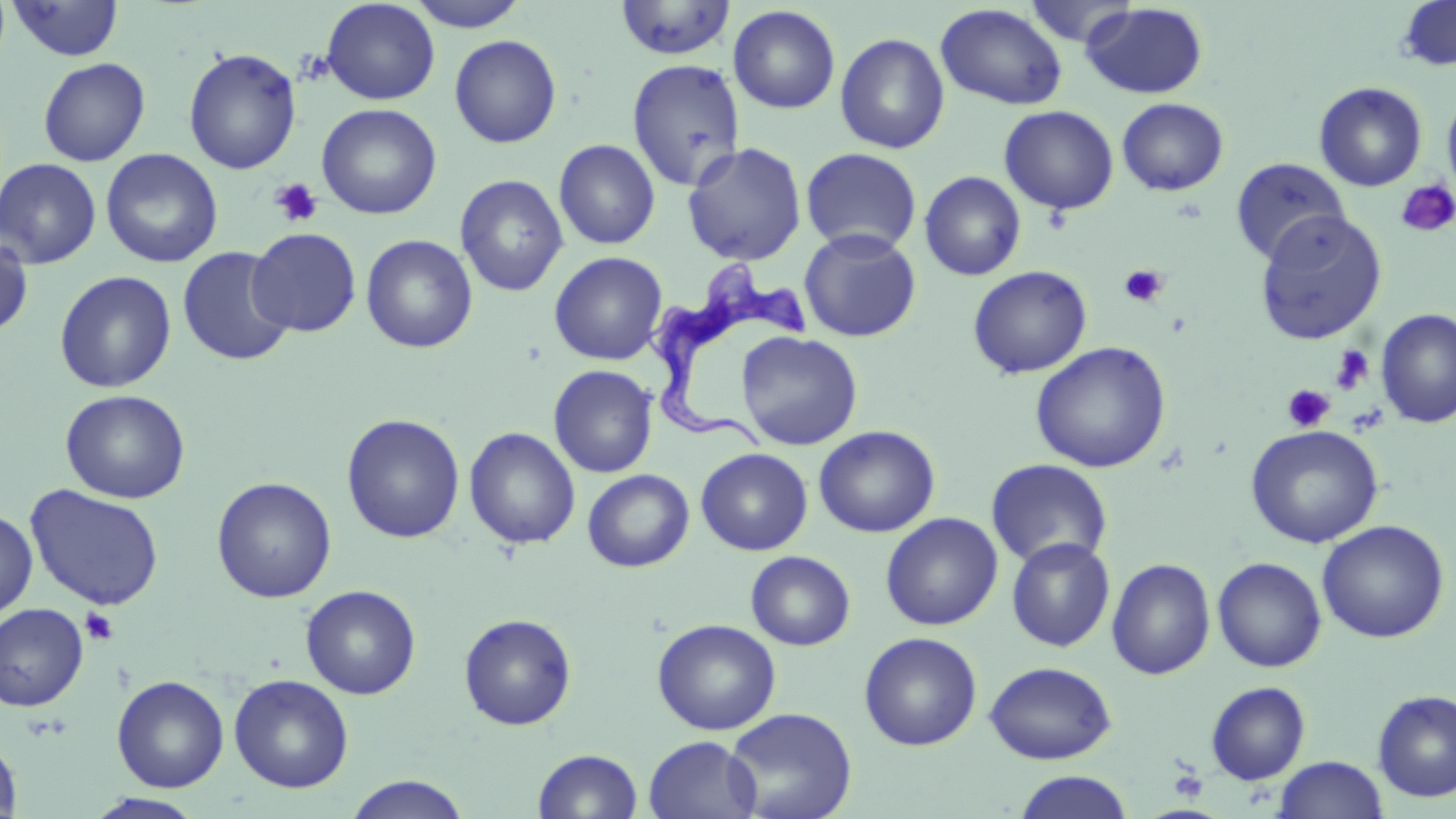
Approximate bounding boxes as (x1, y1, x2, y2) in pixels. Trypanosoma brucei locations: (641, 261, 813, 463). Uninfected red blood cell locations: (320, 0, 440, 105), (407, 0, 531, 32), (1396, 0, 1456, 71), (8, 1, 124, 61), (614, 1, 737, 61), (1025, 1, 1141, 47), (1081, 2, 1208, 99), (935, 3, 1067, 111), (728, 4, 841, 114), (835, 32, 950, 154), (449, 34, 561, 148), (183, 47, 302, 175), (38, 57, 151, 167), (626, 59, 746, 192), (1314, 81, 1427, 192), (1442, 91, 1456, 199), (1117, 98, 1228, 196), (316, 103, 441, 219), (999, 105, 1119, 214), (553, 139, 661, 249), (682, 142, 807, 266), (801, 147, 922, 254), (101, 148, 222, 268), (1230, 157, 1351, 265), (0, 158, 101, 268), (920, 171, 1026, 281), (455, 174, 568, 297), (1255, 210, 1388, 345), (246, 227, 362, 337), (799, 228, 921, 342), (0, 234, 34, 339), (360, 234, 478, 353), (177, 246, 294, 367), (549, 251, 668, 365), (967, 265, 1092, 379), (54, 270, 177, 393), (1375, 308, 1456, 428), (736, 331, 863, 450), (1031, 342, 1171, 473), (548, 365, 658, 478), (60, 389, 191, 504), (341, 413, 465, 544), (1245, 424, 1384, 548), (814, 425, 939, 537), (464, 426, 580, 550), (696, 448, 813, 555), (986, 458, 1113, 570), (582, 469, 694, 572), (211, 476, 337, 603), (26, 485, 165, 610), (0, 509, 38, 620), (881, 513, 1003, 630), (1316, 520, 1450, 643), (1006, 537, 1115, 652), (745, 550, 855, 650), (1212, 556, 1327, 672), (1106, 558, 1216, 680), (301, 585, 421, 699), (0, 603, 88, 711), (458, 613, 577, 730), (652, 618, 781, 735), (859, 631, 982, 751), (984, 661, 1117, 764), (229, 673, 354, 793), (111, 675, 229, 792), (1205, 681, 1311, 785), (1372, 689, 1456, 802), (723, 707, 857, 819), (0, 735, 22, 819), (643, 736, 762, 819), (532, 748, 643, 818), (1274, 755, 1388, 819), (1012, 770, 1136, 818), (344, 775, 472, 818), (85, 793, 206, 818). Platelet locations: (270, 178, 323, 226), (1395, 179, 1456, 239), (1120, 264, 1168, 307), (1330, 344, 1374, 395), (1283, 385, 1335, 432), (80, 608, 119, 645), (1170, 765, 1209, 802). Slide-level diagnosis: Trypanosoma brucei. Image is 1456×819 pixels. Captured at 1000x magnification. May-Grünwald-Giemsa-stained preparation. Light microscopy. Single field of view. Thin blood film.